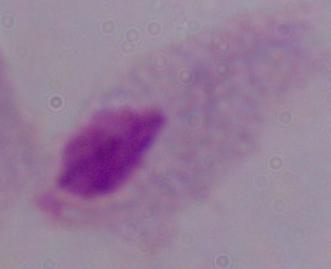

Summary:
  - Modality: photomicrograph
  - Identification: trichomonad
  - Magnification: 1000x